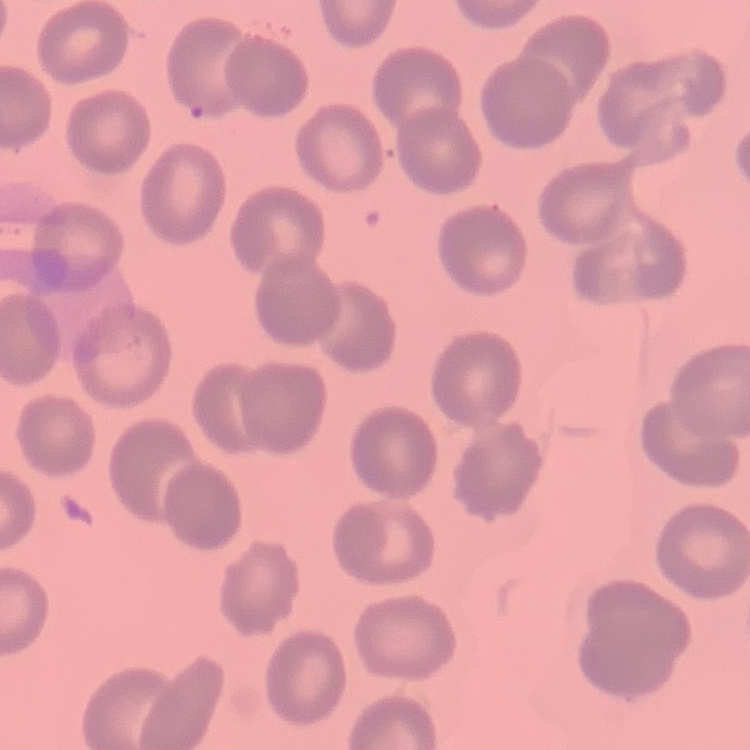
The erythrocytes exhibit no rouleaux formation. Thin peripheral smear. Square crop of a larger photomicrograph. Field's or Giemsa stain.